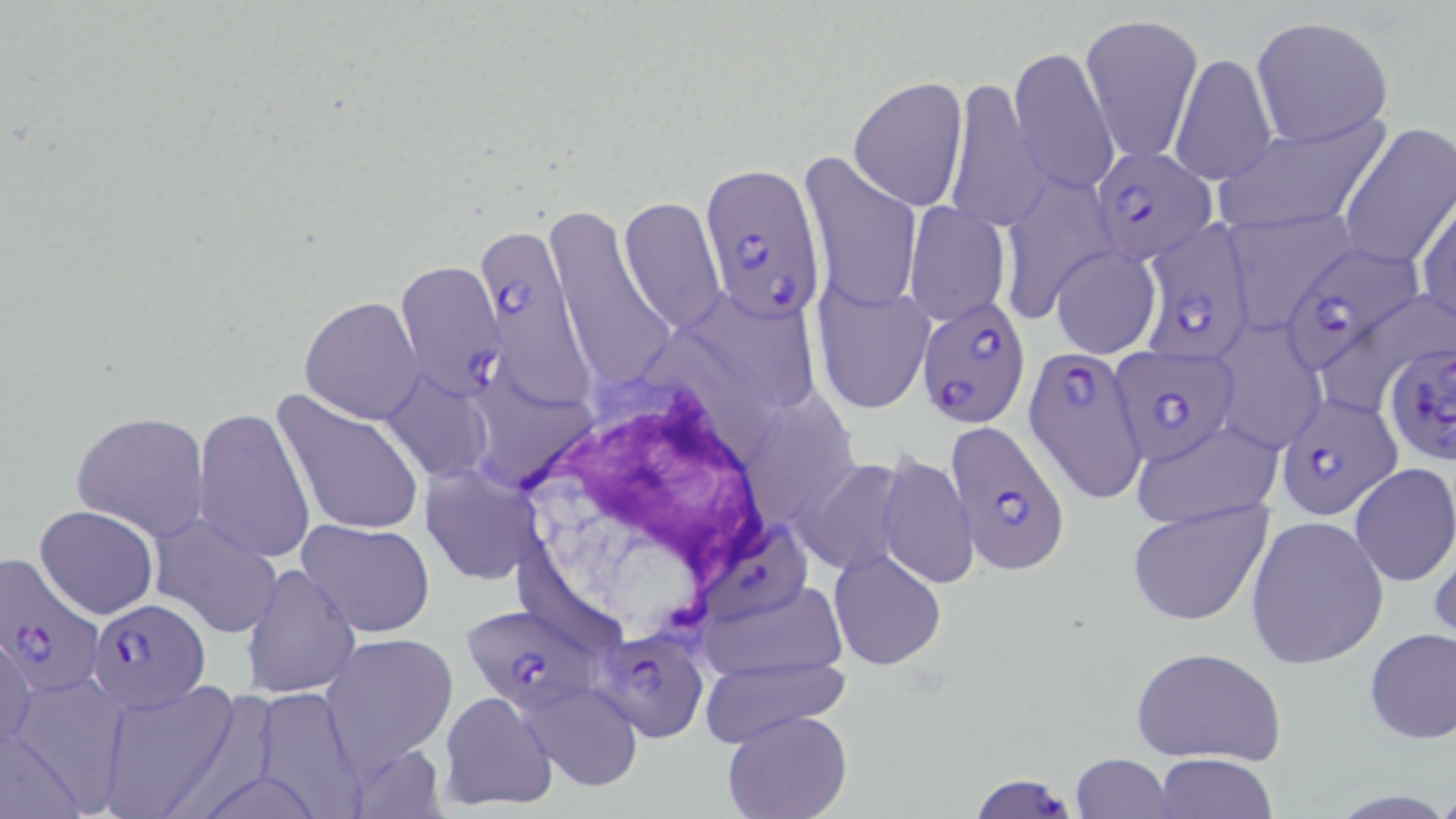

Approximate bounding boxes as [x1, y1, x2, y2] in pixels. White blood cell locations: [511, 381, 800, 650]. Plasmodium falciparum-infected red blood cell locations: [1093, 145, 1216, 272], [699, 161, 828, 327], [1136, 220, 1259, 364], [480, 231, 603, 417], [1277, 244, 1425, 380], [397, 259, 503, 397], [915, 295, 1028, 428], [1387, 340, 1456, 468], [1110, 345, 1240, 465], [1023, 348, 1147, 501], [1276, 393, 1402, 520], [941, 419, 1066, 573], [709, 523, 816, 623], [0, 555, 105, 698], [87, 598, 211, 714], [461, 606, 603, 709], [598, 633, 706, 740], [967, 773, 1080, 819]. Uninfected red blood cell locations: [1081, 11, 1204, 165], [1250, 17, 1393, 147], [1009, 44, 1119, 198], [1169, 51, 1278, 186], [848, 75, 968, 212], [944, 75, 1046, 233], [1211, 112, 1392, 235], [1338, 123, 1454, 273], [798, 152, 922, 315], [999, 168, 1120, 318], [1414, 193, 1455, 331], [618, 197, 725, 332], [904, 201, 1011, 326], [541, 202, 682, 402], [1220, 211, 1360, 329], [1050, 246, 1160, 358], [813, 281, 933, 414], [690, 288, 823, 413], [301, 296, 425, 423], [1210, 327, 1323, 455], [391, 375, 493, 472], [273, 389, 425, 537], [194, 407, 314, 564], [71, 410, 212, 541], [1128, 418, 1284, 530], [876, 451, 977, 590], [808, 458, 909, 568], [1348, 464, 1456, 586], [421, 465, 542, 585], [1126, 498, 1277, 628], [34, 504, 158, 618], [147, 510, 285, 640], [1245, 515, 1388, 669], [298, 519, 436, 638], [1430, 531, 1456, 653], [828, 549, 947, 671], [243, 563, 358, 699], [698, 587, 849, 672], [1362, 627, 1456, 744], [1, 631, 36, 751], [321, 633, 459, 768], [1131, 645, 1287, 767], [698, 658, 850, 745], [4, 678, 127, 812], [97, 678, 244, 818], [520, 684, 643, 789], [438, 690, 560, 813], [722, 710, 852, 819], [1154, 752, 1277, 818], [1070, 753, 1177, 818]. Slide-level diagnosis: Plasmodium falciparum. Image is 1456×819 pixels. Light microscopy. 1000x magnification. One field of a larger specimen. Thin blood film. May-Grünwald-Giemsa stain.